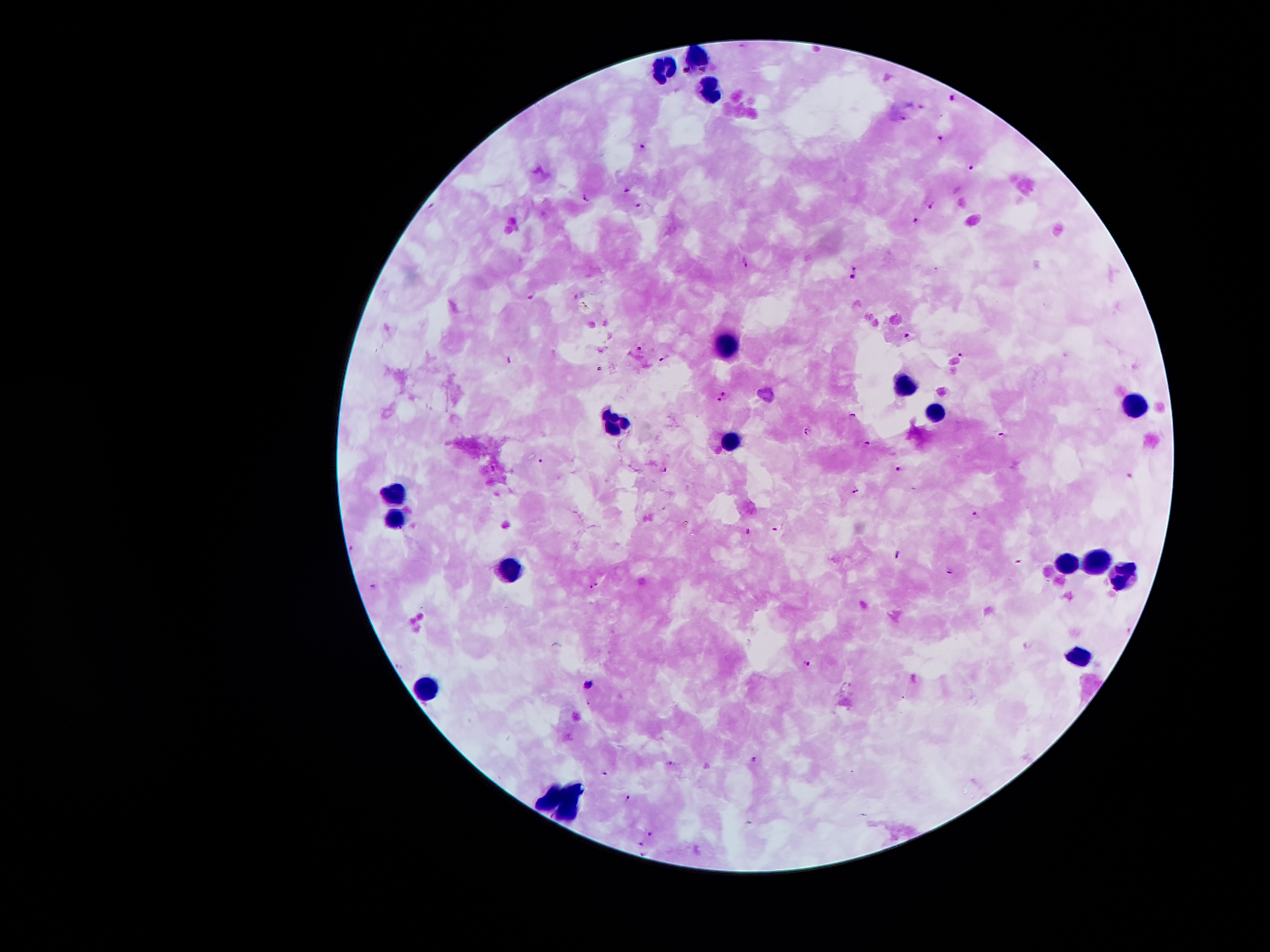
coordinate format = approximate centers as [x, y] in pixels
leukocyte locations = [695, 55], [661, 69], [709, 89], [725, 345], [901, 383], [1134, 403], [937, 411], [612, 421], [730, 440], [394, 494], [394, 515], [1098, 560], [1064, 563], [512, 572], [1123, 573], [1080, 656], [427, 687]
malaria parasite locations = [956, 95], [904, 117], [941, 138], [642, 145], [971, 167], [624, 191], [585, 198], [639, 205], [934, 207], [918, 221], [745, 260], [854, 273], [529, 297], [908, 334], [642, 349], [959, 353], [666, 357], [509, 360], [724, 394], [720, 400], [853, 416], [808, 432], [1003, 436], [866, 443], [540, 461], [898, 467], [664, 470], [856, 491], [974, 514], [776, 530], [748, 531], [899, 553], [1017, 562], [949, 570], [596, 582], [374, 587], [591, 587], [807, 662], [588, 702], [756, 758], [670, 764], [603, 773], [628, 798], [650, 833], [640, 844], [642, 852]
capture = smartphone through the microscope eyepiece
patient malaria status = positive for Plasmodium falciparum
magnification = 100x
stain = Giemsa
image size = 1270×952 pixels
preparation = thick blood film
field of view = one from this slide